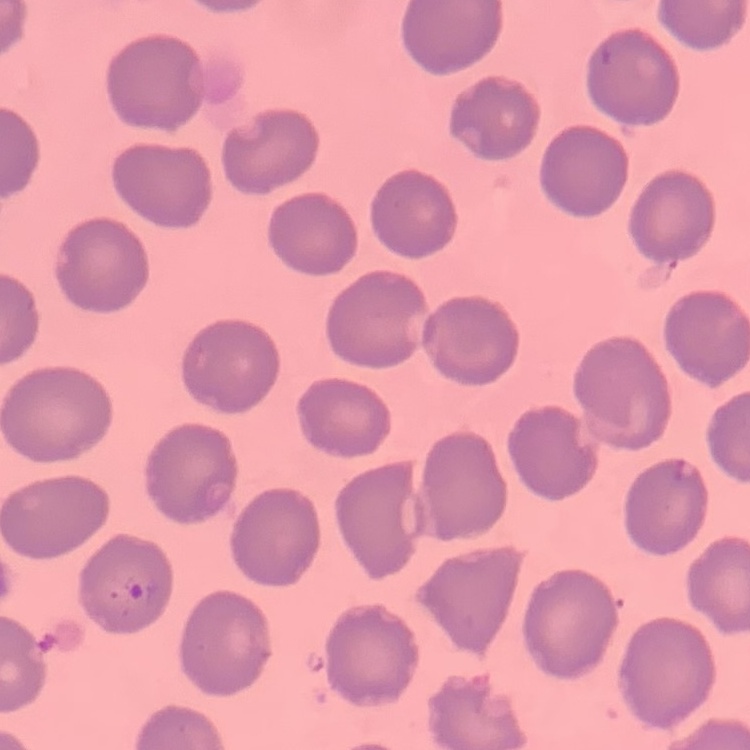
Summary:
  - Erythrocyte morphology: no rouleaux formation
  - Stain: Field's or Giemsa
  - Preparation: thin peripheral smear
  - Image type: square crop of a larger photomicrograph